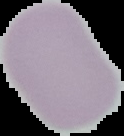
result = negative for malaria parasites
image type = cell region segmented out of the field of view; surrounding area masked to black
image size = 124×136 pixels
preparation = thin blood film